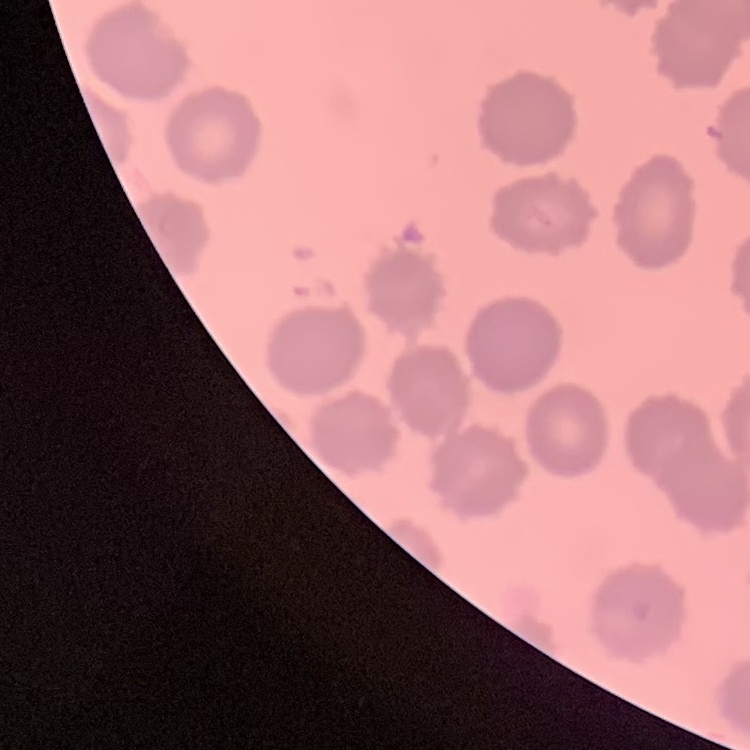

red blood cell morphology = no rouleaux formation
image type = square crop of a larger photomicrograph
preparation = thin blood smear
stain = Field's or Giemsa